Classify this cell by malaria status.
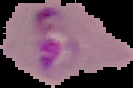
Parasitized.

Summary:
  - Preparation: thin blood film
  - Image size: 133×88 pixels
  - Image type: segmented cell region with the area outside set to black